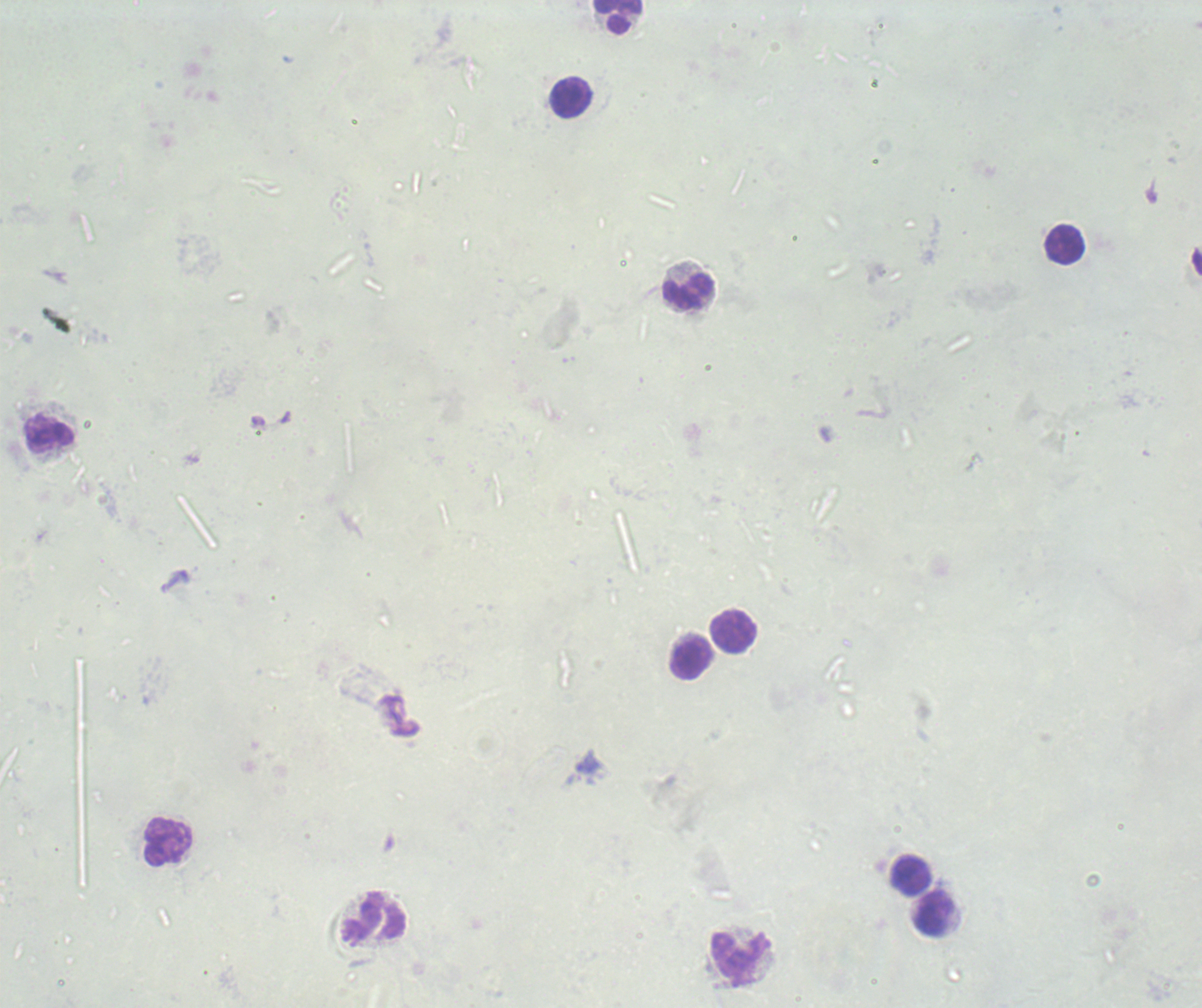
{
  "magnification": "100x",
  "leukocyte_locations": "approximate centers as {x, y} in pixels: {619, 19}, {571, 98}, {1064, 244}, {688, 292}, {50, 434}, {734, 633}, {691, 659}, {168, 842}, {911, 876}, {934, 914}, {375, 919}, {740, 960}",
  "image_size": "1202×1008 pixels",
  "stain": "Romanowsky",
  "field_of_view": "single",
  "background_quality": "unsatisfactory",
  "context": "previously used in an actual diagnosis",
  "preparation": "thick blood smear",
  "result": "no Plasmodium parasites detected"
}